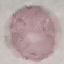
Summary:
  - Malaria status: uninfected
  - Capture: smartphone camera at the microscope eyepiece
  - Preparation: thin blood film
  - Stain: Giemsa
  - Image type: automatically extracted cell patch, resized to 64 × 64 pixels